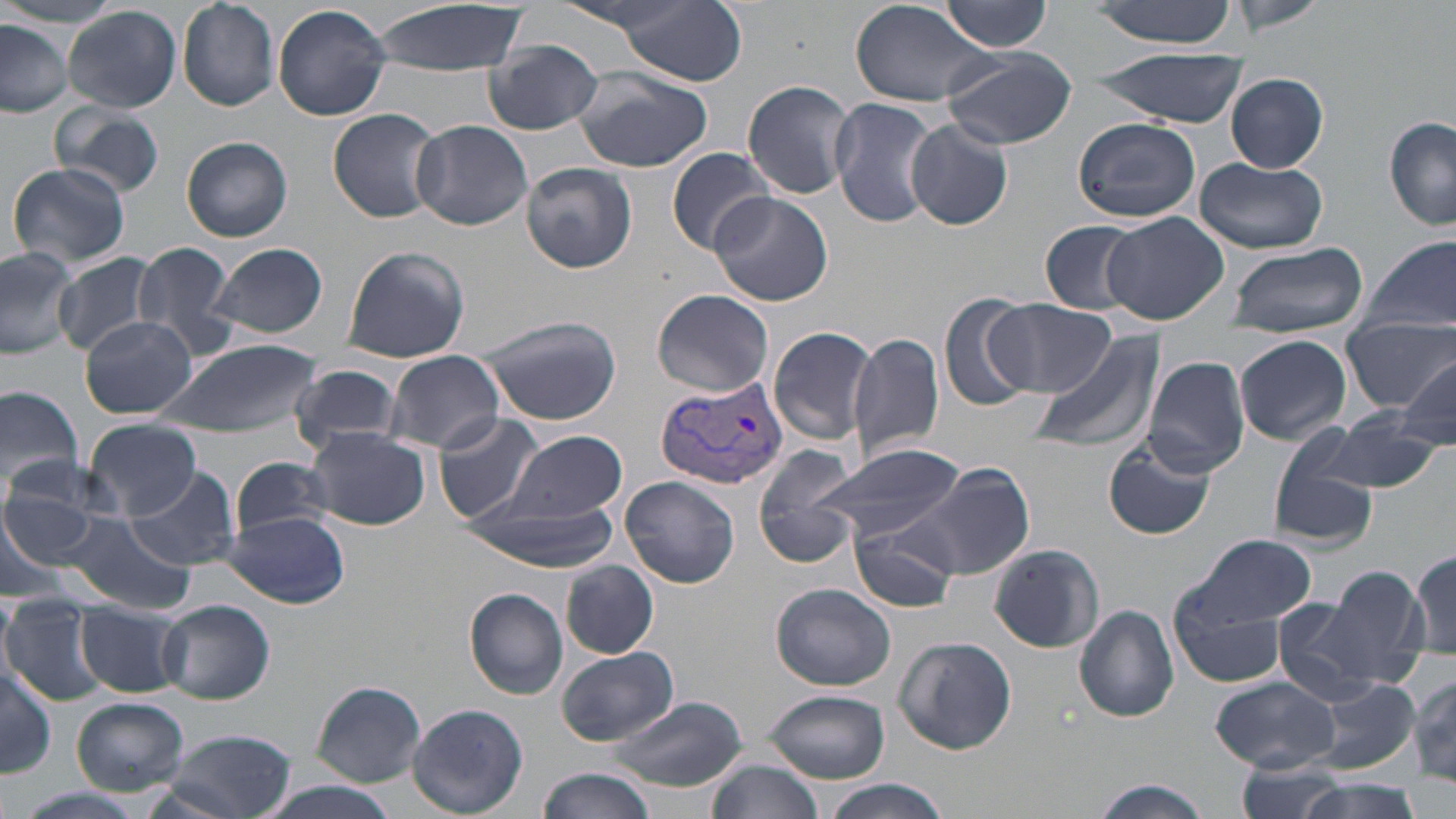

Summary:
  - Coordinate format: approximate bounding boxes as [x1, y1, x2, y2] in pixels
  - Plasmodium vivax-infected red blood cell locations: [655, 374, 790, 490]
  - Uninfected red blood cell locations: [366, 0, 530, 77], [1085, 0, 1245, 47], [1228, 0, 1327, 34], [176, 1, 278, 111], [850, 1, 994, 107], [940, 2, 1054, 53], [612, 3, 746, 85], [272, 4, 392, 121], [62, 5, 181, 113], [0, 19, 74, 116], [484, 42, 604, 136], [940, 47, 1080, 150], [1091, 50, 1247, 126], [571, 67, 718, 175], [1225, 74, 1328, 173], [743, 79, 856, 200], [830, 98, 942, 228], [50, 100, 167, 201], [327, 107, 444, 223], [1384, 116, 1456, 232], [1072, 118, 1200, 223], [412, 119, 533, 232], [904, 119, 1014, 231], [182, 137, 293, 243], [666, 147, 776, 256], [1193, 156, 1328, 252], [6, 162, 132, 272], [521, 162, 637, 274], [709, 192, 836, 308], [1100, 211, 1229, 325], [1041, 222, 1145, 313], [1363, 237, 1455, 338], [130, 239, 242, 361], [208, 242, 328, 340], [1222, 242, 1372, 337], [0, 244, 77, 358], [341, 244, 470, 363], [55, 254, 163, 358], [653, 289, 774, 396], [937, 292, 1039, 412], [984, 299, 1115, 398], [473, 313, 622, 425], [81, 315, 196, 418], [1342, 315, 1452, 413], [767, 326, 879, 446], [848, 330, 945, 462], [1029, 331, 1164, 458], [1235, 334, 1352, 445], [156, 337, 322, 439], [384, 350, 505, 455], [1141, 355, 1251, 478], [1398, 360, 1456, 449], [287, 367, 405, 453], [0, 383, 84, 496], [1322, 410, 1444, 496], [433, 412, 546, 524], [85, 418, 200, 518], [303, 427, 432, 530], [1266, 427, 1381, 550], [499, 430, 627, 525], [1105, 437, 1215, 542], [810, 442, 966, 548], [754, 444, 863, 565], [231, 457, 336, 540], [896, 461, 1036, 583], [124, 466, 243, 570], [622, 475, 740, 588], [0, 487, 108, 588], [459, 493, 621, 572], [52, 511, 196, 615], [219, 511, 351, 607], [850, 517, 959, 614], [1178, 535, 1318, 638], [988, 543, 1103, 654], [1410, 550, 1456, 660], [1359, 553, 1456, 670], [561, 561, 657, 659], [1311, 564, 1428, 687], [770, 582, 896, 691], [464, 588, 569, 699], [0, 590, 18, 687], [1173, 590, 1291, 689], [1269, 594, 1405, 705], [1, 597, 107, 704], [158, 599, 275, 705], [76, 603, 186, 697], [1073, 605, 1181, 723], [891, 636, 1018, 755], [555, 647, 677, 747], [1, 662, 55, 777], [1408, 671, 1456, 787], [1210, 675, 1339, 773], [1304, 675, 1421, 775], [310, 681, 426, 786], [762, 688, 891, 784], [607, 696, 748, 793], [72, 698, 190, 794], [406, 703, 528, 817], [163, 730, 298, 818], [702, 753, 822, 819], [1234, 757, 1351, 819], [536, 767, 655, 819], [1289, 777, 1427, 819], [818, 778, 954, 819], [1086, 779, 1214, 818], [11, 788, 152, 819]
  - Slide-level diagnosis: Plasmodium vivax
  - Magnification: 1000x
  - Image size: 1456×819 pixels
  - Preparation: thin blood film
  - Stain: May-Grünwald-Giemsa
  - Modality: optical microscopy
  - Field of view: one of a larger specimen